Describe the morphology of the erythrocytes.
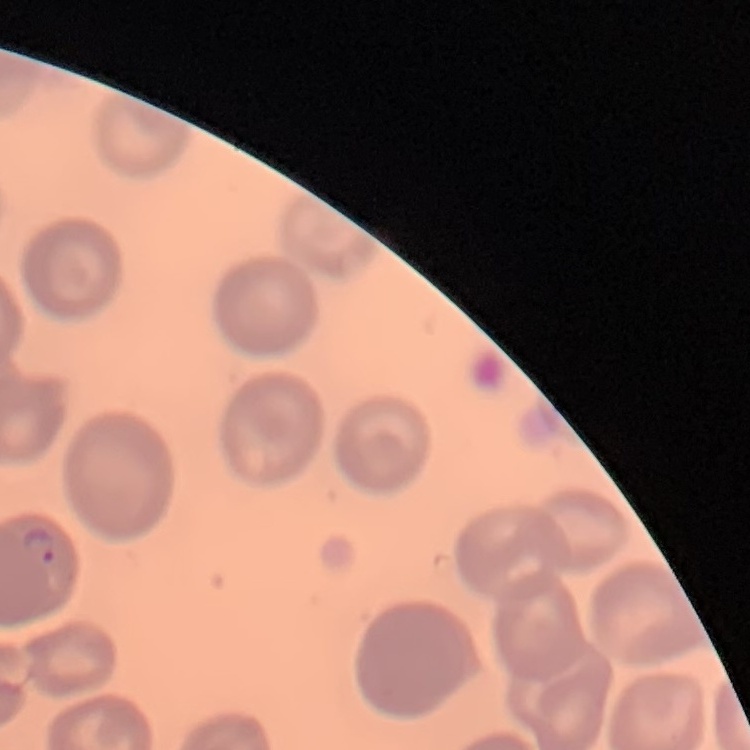
No rouleaux formation.

One tile cut from a larger photomicrograph. Stained with either Field's or Giemsa. Thin blood smear.